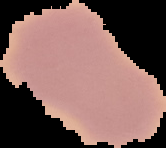 Cell region segmented out of the field of view; the surrounding area is masked to black. Malaria status: uninfected. Image is 166×148 pixels. From a thin blood film.